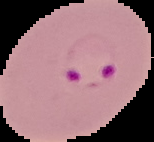
{
  "preparation": "thin blood film",
  "malaria_status": "parasitized",
  "image_size": "154×142 pixels",
  "image_type": "segmented cell region with the area outside set to black"
}